Identify the cell.
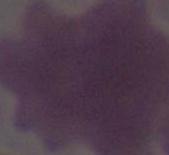
This is an erythrocyte.

Photomicrograph. 1000x magnification.